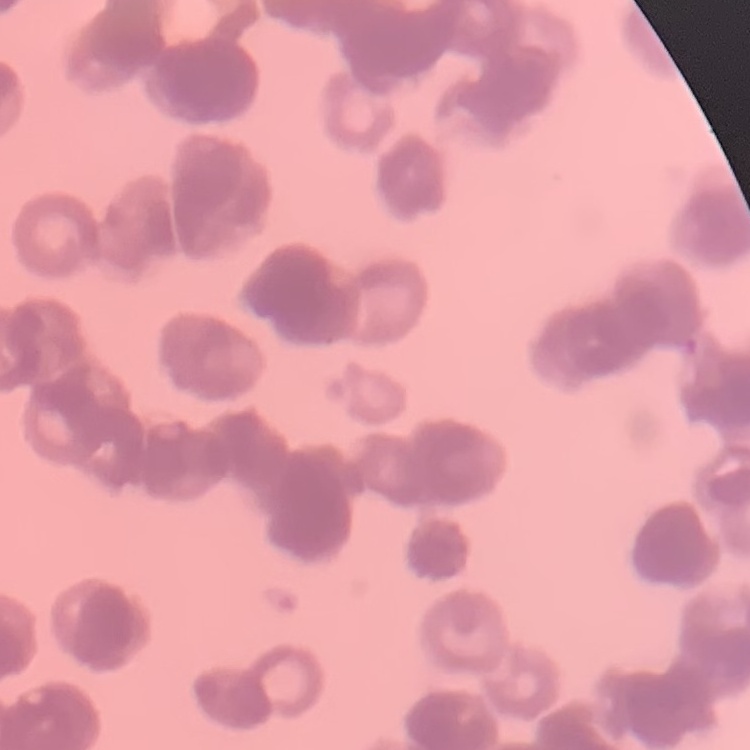
{
  "erythrocyte_morphology": "rouleaux formation",
  "image_type": "one tile cut from a larger photomicrograph",
  "stain": "Field's or Giemsa",
  "preparation": "thin blood smear"
}